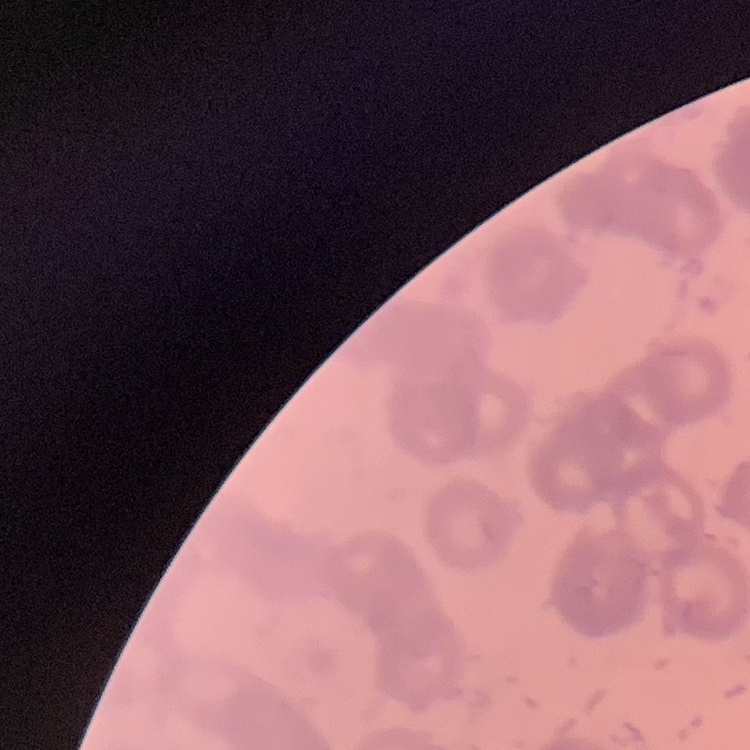

Summary:
  - Red blood cell morphology: rouleaux formation
  - Preparation: thin peripheral smear
  - Image type: square crop of a larger photomicrograph
  - Stain: Field's or Giemsa